Identify the parasite.
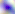
This is Toxoplasma gondii.

400x magnification. Micrograph.